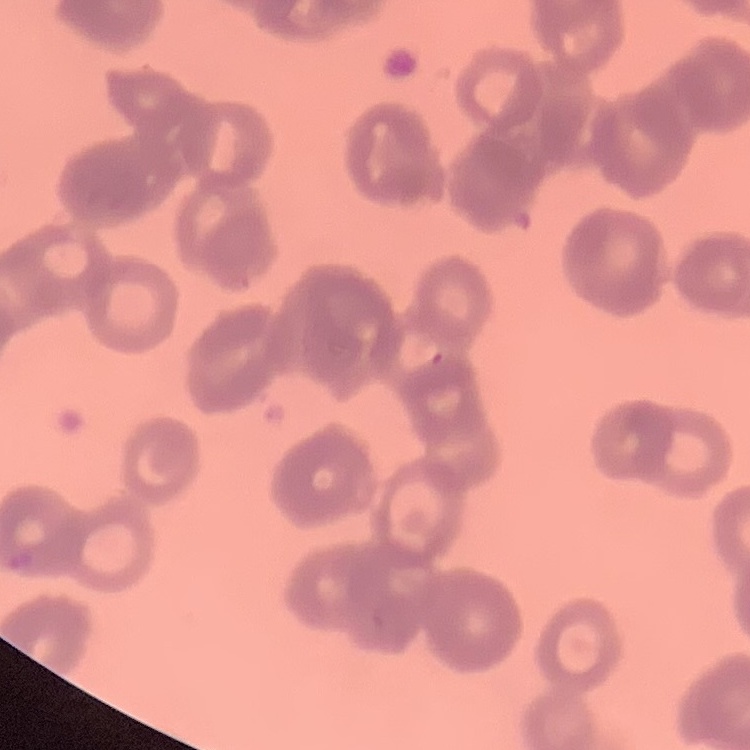

{
  "red_blood_cell_morphology": "rouleaux formation",
  "preparation": "thin blood smear",
  "stain": "Field's or Giemsa",
  "image_type": "square crop of a larger photomicrograph"
}